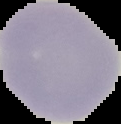
Summary:
  - Result: negative for malaria parasites
  - Image size: 121×124 pixels
  - Preparation: thin blood smear
  - Image type: segmented cell region on a black background